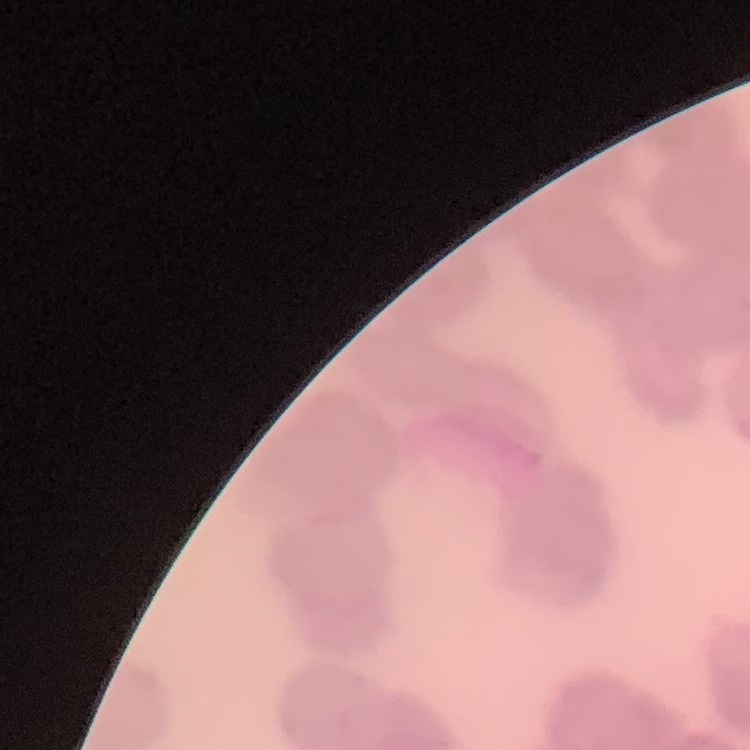

Summary:
  - Red blood cell morphology: rouleaux formation
  - Image type: square crop of a larger photomicrograph
  - Stain: Field's or Giemsa
  - Preparation: thin blood film